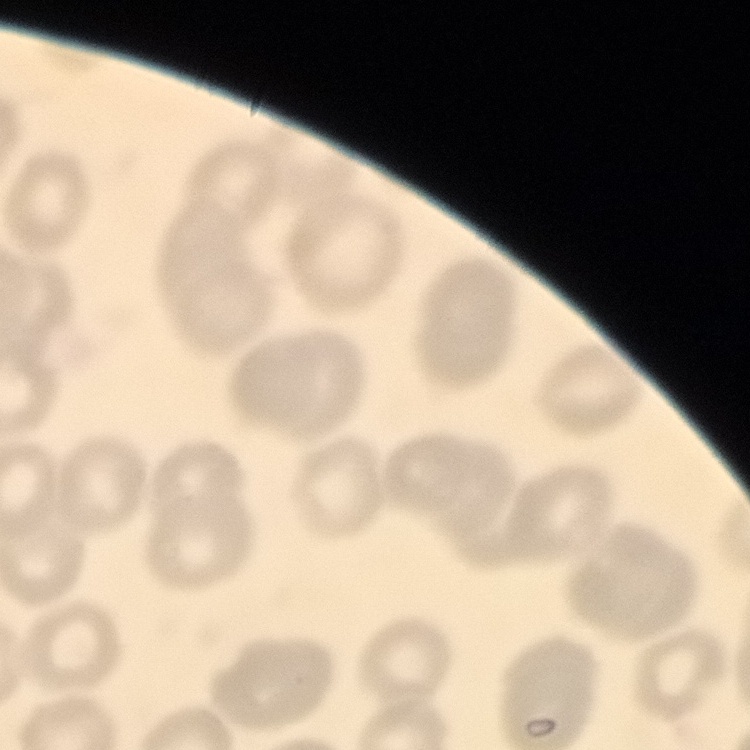
{
  "erythrocyte_morphology": "no rouleaux formation",
  "image_type": "one tile cut from a larger photomicrograph",
  "stain": "Field's or Giemsa",
  "preparation": "thin peripheral smear"
}